Classify this cell by malaria status.
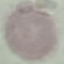

Uninfected.

Giemsa stain. Photographed with a smartphone camera at the microscope eyepiece. Automatically extracted cell patch, resized to 64 × 64 pixels. Thin blood film.